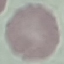
{
  "result": "no malaria parasites seen",
  "preparation": "thin blood smear",
  "capture": "smartphone camera at the microscope eyepiece",
  "stain": "Giemsa",
  "image_type": "automatically extracted cell patch, resized to 64 × 64 pixels"
}